Give the preparation type.
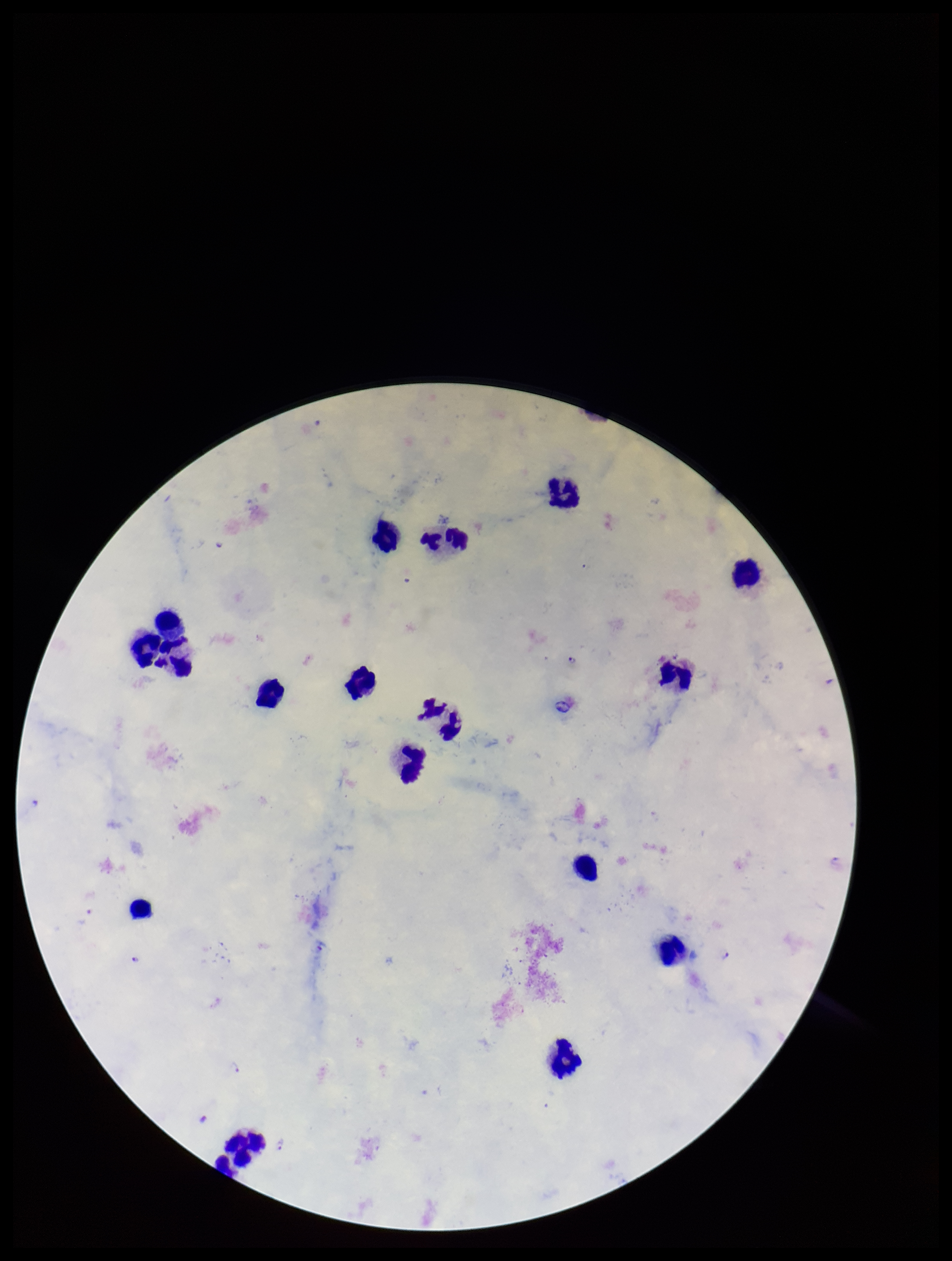
It is a thick blood smear.

Giemsa stain. Photographed through the microscope eyepiece with a smartphone camera. Single field of view. Species reported for this patient: Plasmodium falciparum. Image is 952×1261 pixels. Leukocyte count: 16. Plasmodium parasites: detected. Parasite count: 2. Patient malaria status: infected.